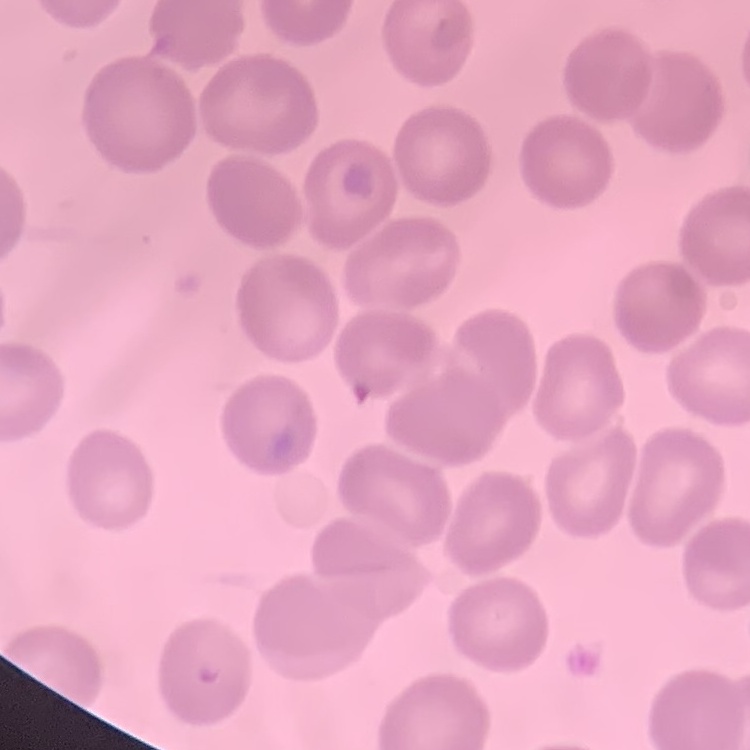
red blood cell morphology = no rouleaux formation
preparation = thin blood film
stain = Field's or Giemsa
image type = square crop of a larger photomicrograph